Identify the parasite.
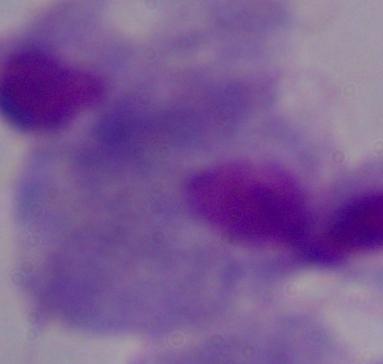

A trichomonad.

Micrograph. 1000x magnification.